Assess for Plasmodium parasites.
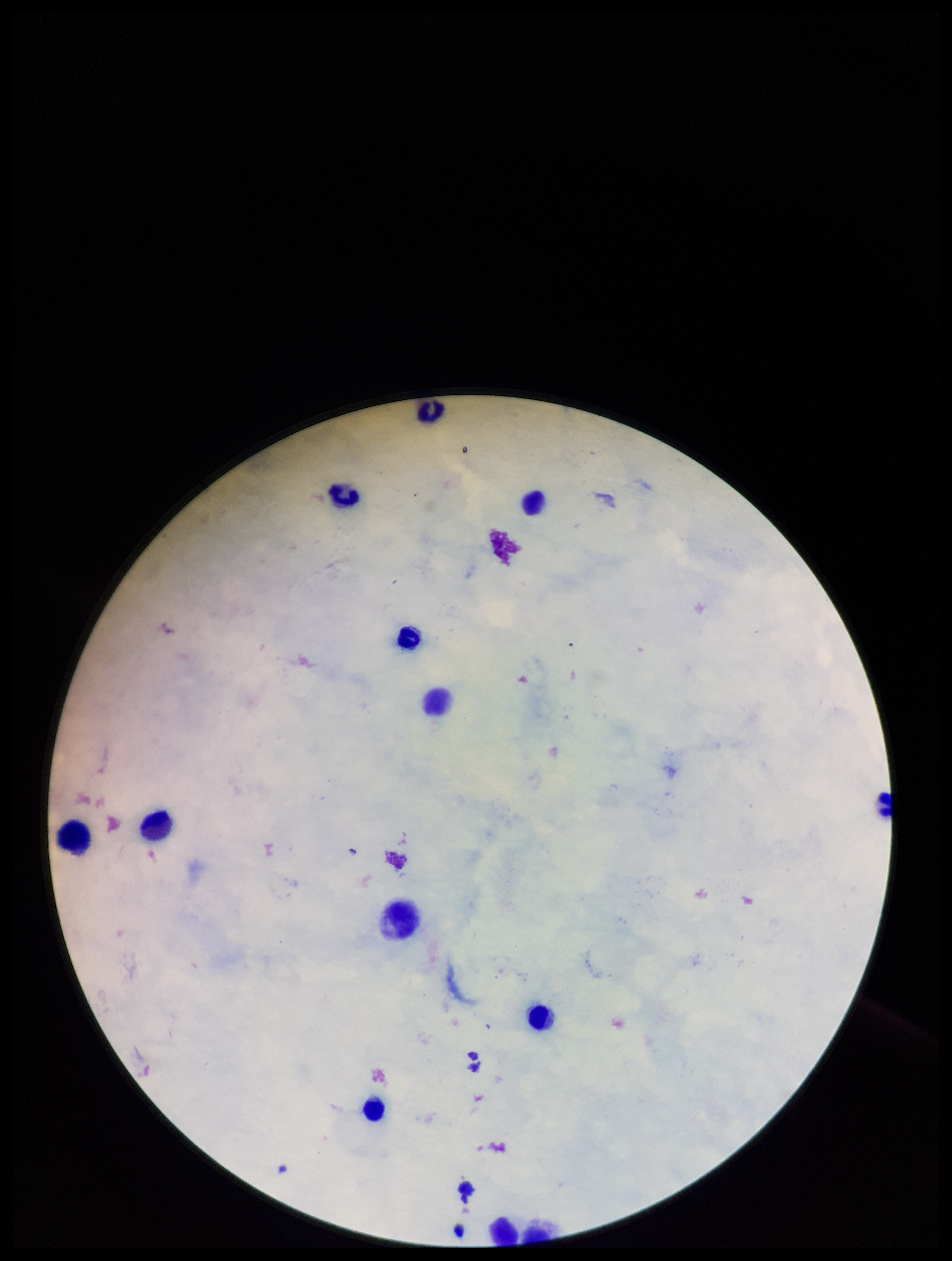
None seen.

{
  "parasite_count": 0,
  "image_size": "952×1261 pixels",
  "capture": "smartphone photograph through the microscope eyepiece",
  "leukocyte_count": 12,
  "patient_malaria_status": "negative",
  "stain": "Giemsa",
  "preparation": "thick smear",
  "field_of_view": "single"
}